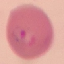

Summary:
  - Result: malaria parasites identified
  - Preparation: thin smear
  - Image type: automatically extracted cell patch, resized to 64 × 64 pixels
  - Stain: Giemsa
  - Capture: smartphone camera at the microscope eyepiece